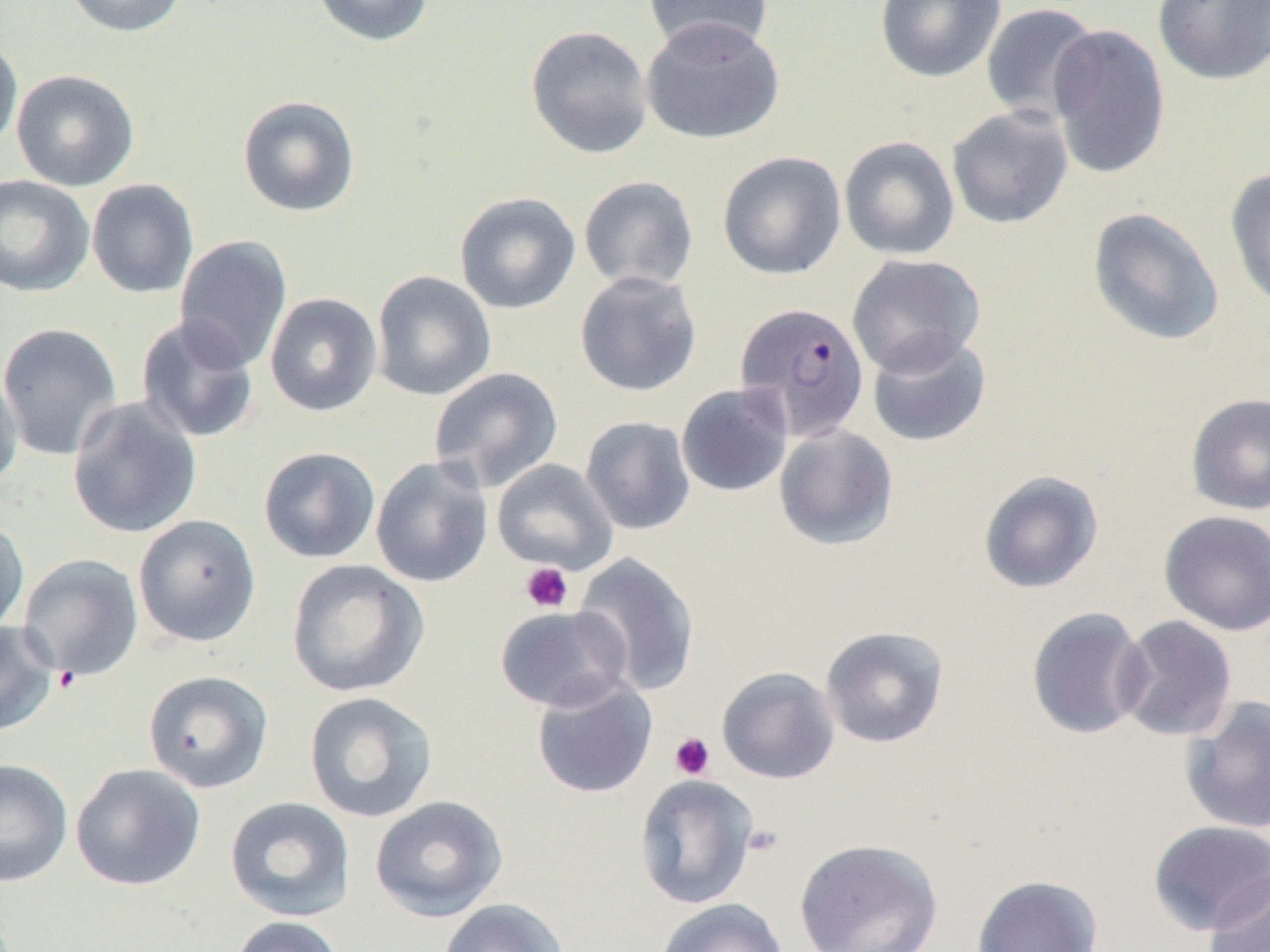
slide_level_diagnosis: Plasmodium falciparum
modality: optical microscopy
preparation: thin blood smear
platelet_locations: 'approximate bounding boxes as (x1, y1, x2, y2) in pixels: (520, 562, 573, 613), (669, 733, 715, 780), (742, 823, 784, 859)'
plasmodium_falciparum_infected_red_blood_cell_locations: 'approximate bounding boxes as (x1, y1, x2, y2) in pixels: (734, 302, 870, 442)'
field_of_view: one of a larger specimen
uninfected_red_blood_cell_locations: 'approximate bounding boxes as (x1, y1, x2, y2) in pixels: (65, 0, 187, 37), (312, 0, 434, 47), (875, 0, 1005, 83), (1153, 0, 1270, 85), (643, 1, 774, 57), (980, 3, 1101, 124), (640, 17, 784, 144), (1047, 23, 1172, 180), (525, 25, 653, 159), (0, 37, 23, 159), (11, 69, 139, 191), (237, 94, 361, 217), (947, 105, 1074, 229), (839, 136, 960, 261), (717, 151, 846, 280), (1224, 167, 1270, 310), (0, 175, 95, 297), (578, 176, 699, 293), (86, 178, 199, 299), (455, 192, 581, 314), (1087, 207, 1224, 346), (174, 235, 293, 372), (846, 253, 985, 376), (574, 270, 702, 397), (370, 271, 497, 401), (264, 292, 382, 416), (135, 316, 260, 444), (0, 322, 123, 461), (867, 331, 992, 447), (428, 367, 564, 493), (0, 368, 23, 496), (676, 383, 793, 497), (1185, 393, 1270, 515), (67, 398, 202, 539), (581, 416, 695, 535), (774, 423, 899, 551), (258, 446, 381, 564), (371, 455, 494, 588), (491, 458, 618, 575), (978, 470, 1104, 594), (1158, 510, 1270, 636), (0, 515, 30, 636), (133, 515, 261, 647), (573, 552, 700, 697), (18, 554, 144, 681), (286, 559, 429, 698), (494, 604, 633, 713), (1026, 606, 1151, 740), (1115, 615, 1237, 741), (0, 620, 59, 737), (820, 626, 949, 748), (716, 666, 840, 784), (143, 669, 274, 793), (531, 677, 658, 799), (303, 691, 439, 823), (1180, 694, 1270, 834), (0, 758, 73, 887), (70, 763, 206, 891), (633, 773, 759, 910), (224, 796, 355, 921), (369, 796, 508, 922), (1147, 820, 1270, 935), (793, 838, 944, 952), (1203, 871, 1270, 951), (971, 875, 1103, 952), (438, 898, 569, 952), (654, 898, 789, 952), (228, 916, 346, 952)'
image_size: 1270×952 pixels
magnification: 1000x